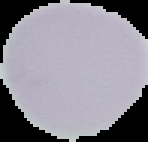 Segmented cell region on a black background. From a thin blood smear. Malaria status: uninfected. Image is 148×142 pixels.